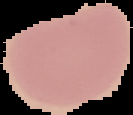
malaria status = uninfected
image size = 133×115 pixels
image type = segmented cell region with the area outside set to black
preparation = thin blood film